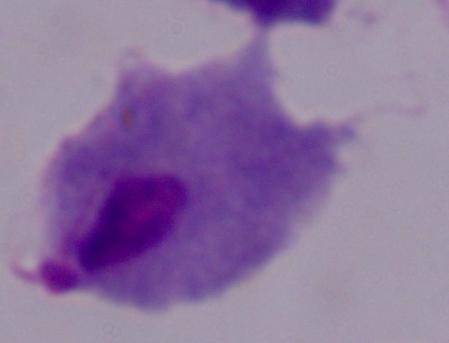
{
  "magnification": "1000x",
  "identification": "trichomonad",
  "modality": "photomicrograph"
}